Assess this cell for malaria.
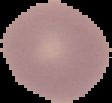
Uninfected.

Cell region segmented out of the field of view; the surrounding area is masked to black. Image is 112×103 pixels. From a thin blood smear.